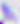
Summary:
  - Magnification: 400x
  - Modality: photomicrograph
  - Identification: Toxoplasma gondii